Name the parasite shown.
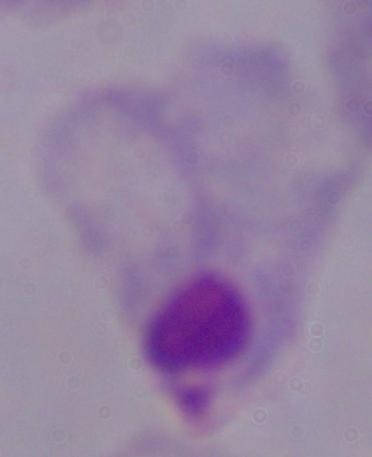

A trichomonad.

Photomicrograph. Captured at 1000x magnification.